Assess this cell for malaria.
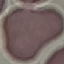

It is uninfected.

Summary:
  - Image type: automatically extracted cell patch, resized to 64 × 64 pixels
  - Stain: Giemsa
  - Preparation: thin smear
  - Capture: smartphone camera at the microscope eyepiece